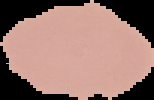
{
  "result": "no Plasmodium parasites detected",
  "image_size": "154×100 pixels",
  "preparation": "thin blood smear",
  "image_type": "segmented cell region on a black background"
}